Assess this cell for malaria.
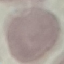
Uninfected.

Giemsa-stained preparation. Thin smear of blood. Acquired by smartphone through the microscope eyepiece. Cell patch, automatically extracted from a larger field of view and resized to 64 × 64 pixels.